Classify this cell by malaria status.
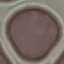
It is uninfected.

Acquired by smartphone through the microscope eyepiece. Giemsa stain. Thin smear of blood. Cell patch, automatically extracted from a larger field of view and resized to 64 × 64 pixels.